State which cell type is depicted.
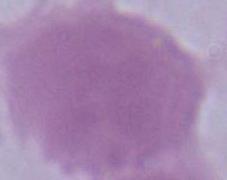

This is an erythrocyte.

magnification: 1000x
modality: photomicrograph